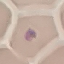

Summary:
  - Result: no malaria parasites seen
  - Preparation: thin smear
  - Capture: smartphone through the microscope eyepiece
  - Image type: automatically extracted cell patch, resized to 64 × 64 pixels
  - Stain: Giemsa